Locate every Plasmodium falciparum-infected red blood cell.
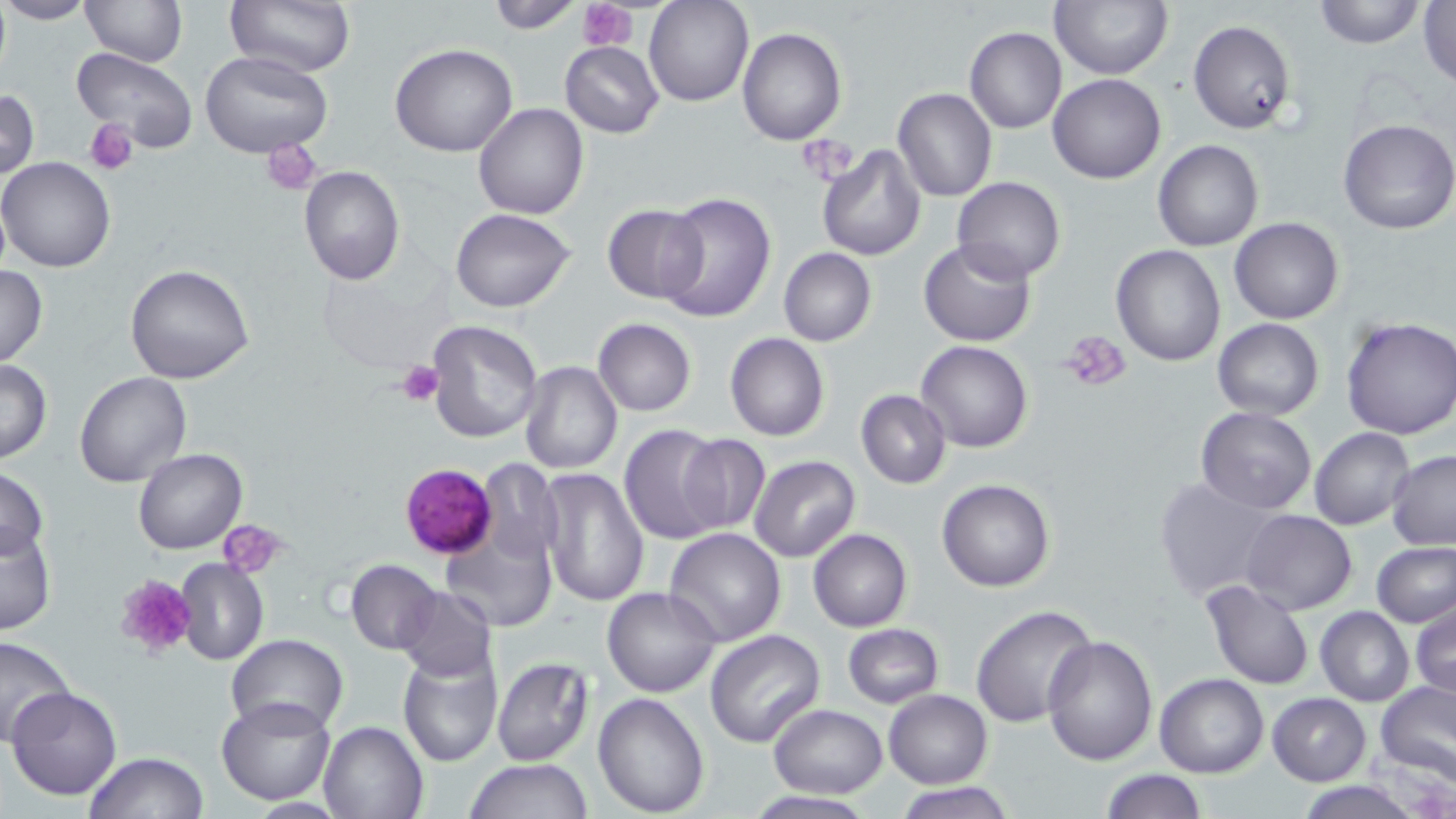
Approximate bounding boxes as named x1/y1/x2/y2 corners in pixels.
Plasmodium falciparum-infected red blood cells: (x1=398, y1=462, x2=497, y2=560).

Summary:
  - Uninfected red blood cell locations: (x1=0, y1=0, x2=95, y2=26), (x1=79, y1=0, x2=187, y2=67), (x1=224, y1=0, x2=355, y2=77), (x1=485, y1=0, x2=583, y2=32), (x1=645, y1=0, x2=753, y2=106), (x1=1310, y1=0, x2=1425, y2=49), (x1=1049, y1=1, x2=1173, y2=80), (x1=1418, y1=1, x2=1455, y2=90), (x1=1188, y1=20, x2=1295, y2=134), (x1=966, y1=26, x2=1066, y2=133), (x1=737, y1=28, x2=847, y2=146), (x1=560, y1=40, x2=664, y2=138), (x1=390, y1=42, x2=518, y2=158), (x1=71, y1=48, x2=199, y2=152), (x1=201, y1=51, x2=333, y2=160), (x1=1048, y1=73, x2=1165, y2=184), (x1=0, y1=87, x2=39, y2=181), (x1=893, y1=88, x2=998, y2=202), (x1=473, y1=102, x2=589, y2=219), (x1=1337, y1=119, x2=1456, y2=235), (x1=1153, y1=140, x2=1262, y2=252), (x1=816, y1=146, x2=924, y2=261), (x1=1, y1=157, x2=118, y2=273), (x1=298, y1=165, x2=404, y2=285), (x1=952, y1=177, x2=1065, y2=282), (x1=656, y1=192, x2=776, y2=324), (x1=603, y1=205, x2=706, y2=304), (x1=451, y1=208, x2=576, y2=313), (x1=1230, y1=216, x2=1344, y2=324), (x1=918, y1=239, x2=1036, y2=347), (x1=1112, y1=244, x2=1227, y2=366), (x1=777, y1=248, x2=876, y2=347), (x1=0, y1=263, x2=47, y2=368), (x1=124, y1=264, x2=254, y2=384), (x1=1340, y1=315, x2=1456, y2=440), (x1=592, y1=318, x2=696, y2=416), (x1=1212, y1=318, x2=1324, y2=419), (x1=426, y1=320, x2=542, y2=442), (x1=725, y1=333, x2=830, y2=441), (x1=916, y1=341, x2=1033, y2=452), (x1=0, y1=360, x2=53, y2=464), (x1=518, y1=360, x2=622, y2=474), (x1=74, y1=372, x2=191, y2=489), (x1=856, y1=389, x2=952, y2=488), (x1=1195, y1=407, x2=1318, y2=512), (x1=619, y1=423, x2=728, y2=542), (x1=1308, y1=427, x2=1414, y2=530), (x1=676, y1=434, x2=771, y2=534), (x1=134, y1=447, x2=247, y2=553), (x1=1386, y1=450, x2=1456, y2=550), (x1=749, y1=456, x2=860, y2=562), (x1=475, y1=461, x2=562, y2=568), (x1=0, y1=467, x2=49, y2=564), (x1=537, y1=467, x2=649, y2=608), (x1=1155, y1=476, x2=1278, y2=601), (x1=937, y1=478, x2=1056, y2=592), (x1=1241, y1=509, x2=1356, y2=614), (x1=441, y1=522, x2=557, y2=631), (x1=0, y1=525, x2=56, y2=633), (x1=663, y1=528, x2=786, y2=646), (x1=808, y1=528, x2=912, y2=631), (x1=1371, y1=541, x2=1456, y2=628), (x1=346, y1=559, x2=442, y2=655), (x1=176, y1=560, x2=269, y2=666), (x1=1200, y1=580, x2=1314, y2=689), (x1=394, y1=585, x2=497, y2=681), (x1=602, y1=587, x2=723, y2=697), (x1=1410, y1=596, x2=1455, y2=701), (x1=970, y1=604, x2=1096, y2=728), (x1=1315, y1=606, x2=1414, y2=706), (x1=842, y1=622, x2=944, y2=707), (x1=705, y1=630, x2=824, y2=748), (x1=1043, y1=633, x2=1158, y2=764), (x1=225, y1=635, x2=348, y2=736), (x1=0, y1=636, x2=75, y2=747), (x1=397, y1=650, x2=502, y2=768), (x1=491, y1=657, x2=595, y2=767), (x1=1155, y1=673, x2=1268, y2=777), (x1=1375, y1=680, x2=1456, y2=785), (x1=6, y1=685, x2=123, y2=801), (x1=883, y1=690, x2=992, y2=789), (x1=592, y1=691, x2=709, y2=815), (x1=1268, y1=692, x2=1370, y2=784), (x1=215, y1=696, x2=338, y2=805), (x1=768, y1=704, x2=887, y2=796), (x1=316, y1=719, x2=430, y2=819), (x1=85, y1=752, x2=209, y2=819), (x1=466, y1=758, x2=594, y2=818), (x1=1099, y1=770, x2=1207, y2=818), (x1=1295, y1=781, x2=1424, y2=818), (x1=897, y1=783, x2=1015, y2=819), (x1=743, y1=791, x2=879, y2=819)
  - Platelet locations: (x1=580, y1=0, x2=636, y2=50), (x1=87, y1=119, x2=139, y2=176), (x1=803, y1=139, x2=858, y2=180), (x1=263, y1=142, x2=323, y2=196), (x1=1059, y1=330, x2=1133, y2=394), (x1=400, y1=362, x2=442, y2=407), (x1=223, y1=521, x2=289, y2=580), (x1=112, y1=573, x2=198, y2=662)
  - Slide-level diagnosis: Plasmodium falciparum
  - Stain: May-Grünwald-Giemsa
  - Magnification: 1000x
  - Modality: optical microscopy
  - Preparation: thin blood film
  - Image size: 1456×819 pixels
  - Field of view: one of a larger specimen